Outline each Plasmodium falciparum-infected red blood cell.
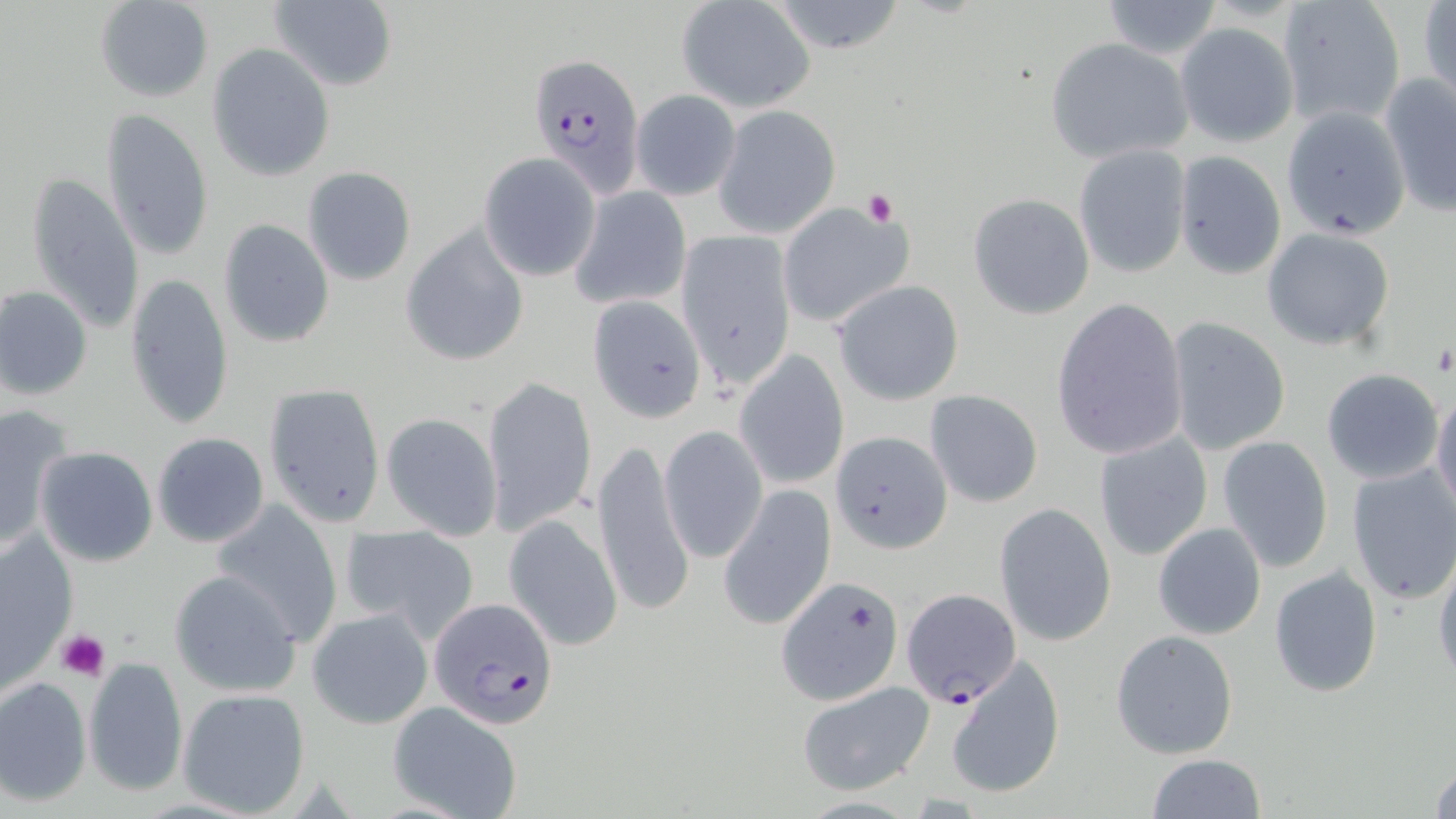
Approximate bounding boxes as (x1, y1, x2, y2) in pixels.
Plasmodium falciparum-infected red blood cells: (531, 49, 645, 200), (901, 589, 1023, 706), (428, 597, 559, 729).

Uninfected red blood cell locations: (95, 0, 213, 102), (268, 0, 398, 91), (1277, 0, 1405, 128), (676, 1, 815, 112), (768, 1, 908, 54), (1100, 1, 1226, 59), (1418, 2, 1456, 108), (1174, 23, 1298, 147), (1046, 38, 1193, 164), (208, 43, 335, 181), (1380, 72, 1456, 216), (630, 88, 741, 202), (718, 106, 842, 238), (101, 109, 212, 261), (1074, 144, 1192, 279), (477, 150, 602, 281), (1173, 152, 1286, 280), (302, 167, 416, 286), (28, 171, 145, 335), (571, 184, 691, 309), (968, 193, 1094, 319), (777, 201, 915, 328), (219, 219, 336, 350), (400, 223, 531, 367), (1263, 229, 1395, 350), (675, 230, 797, 390), (124, 273, 235, 430), (832, 280, 965, 406), (0, 286, 91, 401), (1050, 295, 1190, 463), (588, 296, 707, 425), (1165, 317, 1291, 456), (734, 351, 850, 490), (1320, 368, 1445, 485), (482, 376, 595, 538), (262, 383, 387, 526), (1431, 387, 1456, 519), (924, 389, 1045, 507), (0, 403, 72, 551), (380, 412, 503, 540), (659, 425, 767, 563), (831, 429, 950, 555), (1093, 432, 1214, 562), (152, 433, 269, 547), (1217, 435, 1335, 573), (593, 436, 695, 620), (35, 446, 158, 567), (1345, 464, 1456, 606), (718, 484, 836, 631), (210, 501, 344, 644), (993, 501, 1117, 647), (503, 513, 625, 651), (1154, 522, 1266, 640), (341, 524, 480, 644), (1, 531, 75, 692), (1432, 554, 1456, 686), (1269, 565, 1383, 697), (167, 570, 302, 698), (777, 574, 907, 706), (307, 608, 434, 728), (1110, 630, 1238, 759), (945, 654, 1065, 799), (83, 655, 189, 796), (0, 676, 92, 805), (795, 681, 935, 797), (178, 688, 311, 817), (389, 702, 523, 819), (1146, 754, 1267, 818), (1429, 758, 1456, 818). Platelet locations: (861, 187, 896, 228), (1431, 343, 1455, 375), (57, 629, 111, 682). Slide-level diagnosis: Plasmodium falciparum. Single field of view. May-Grünwald-Giemsa-stained preparation. Image is 1456×819 pixels. 1000x magnification. Thin blood smear. Optical microscopy.